Classify this cell by malaria status.
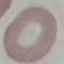
Uninfected.

Cell patch, automatically extracted from a larger field of view and resized to 64 × 64 pixels. Thin smear of blood. Giemsa-stained preparation. Photographed with a smartphone camera at the microscope eyepiece.